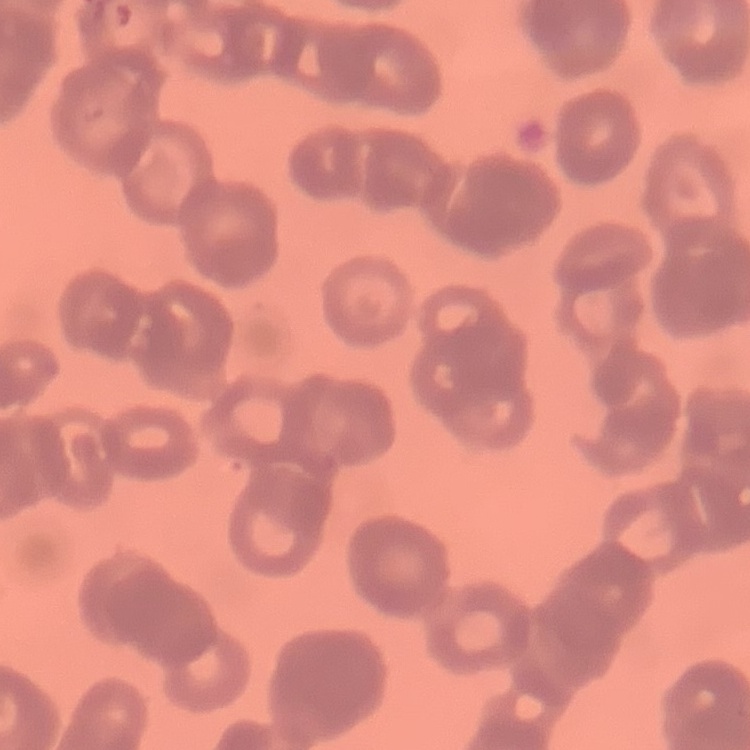
Summary:
  - Erythrocyte morphology: rouleaux formation
  - Image type: one tile cut from a larger photomicrograph
  - Stain: Field's or Giemsa
  - Preparation: thin blood film